Describe the morphology of the erythrocytes.
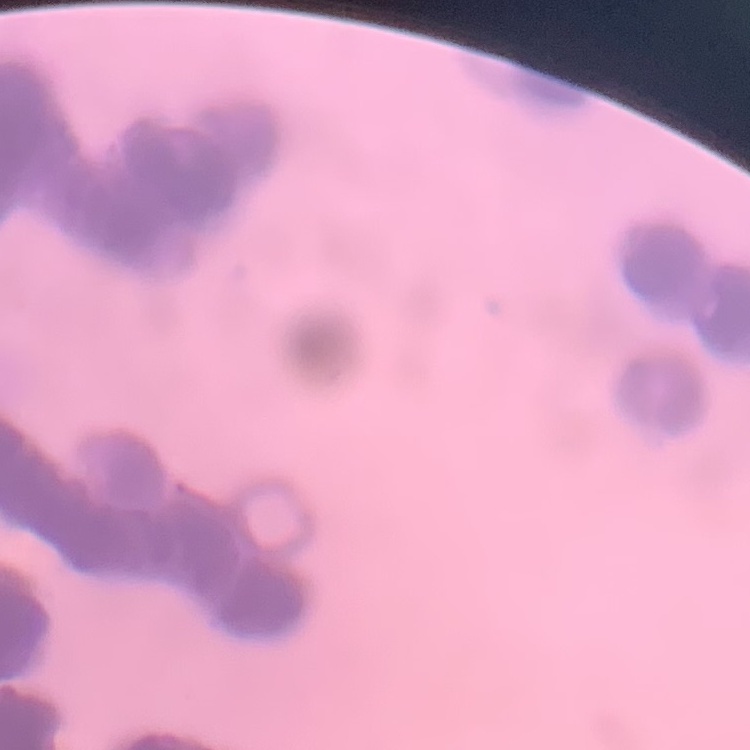
They show rouleaux formation.

Summary:
  - Image type: square crop of a larger photomicrograph
  - Stain: Field's or Giemsa
  - Preparation: thin blood film